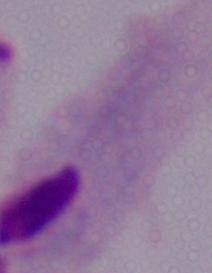
{
  "magnification": "1000x",
  "identification": "trichomonad",
  "modality": "micrograph"
}